Identify the parasite.
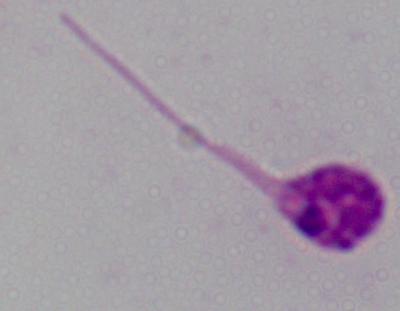
This is Leishmania.

Summary:
  - Magnification: 1000x
  - Modality: micrograph